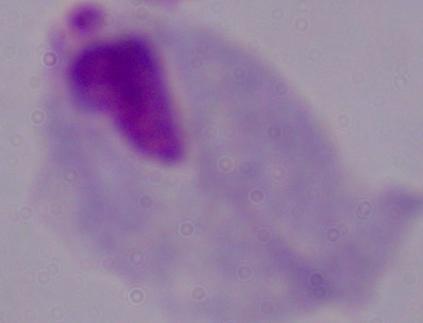 Captured at 1000x magnification. Micrograph. A trichomonad is shown.